Assess this cell for malaria.
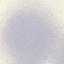
Uninfected.

{
  "stain": "Giemsa",
  "image_type": "automatically extracted cell patch, resized to 64 × 64 pixels",
  "preparation": "thin blood film",
  "capture": "smartphone through the microscope eyepiece"
}